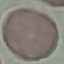

result = no malaria parasites detected
capture = smartphone camera at the microscope eyepiece
preparation = thin blood smear
image type = automatically extracted cell patch, resized to 64 × 64 pixels
stain = Giemsa